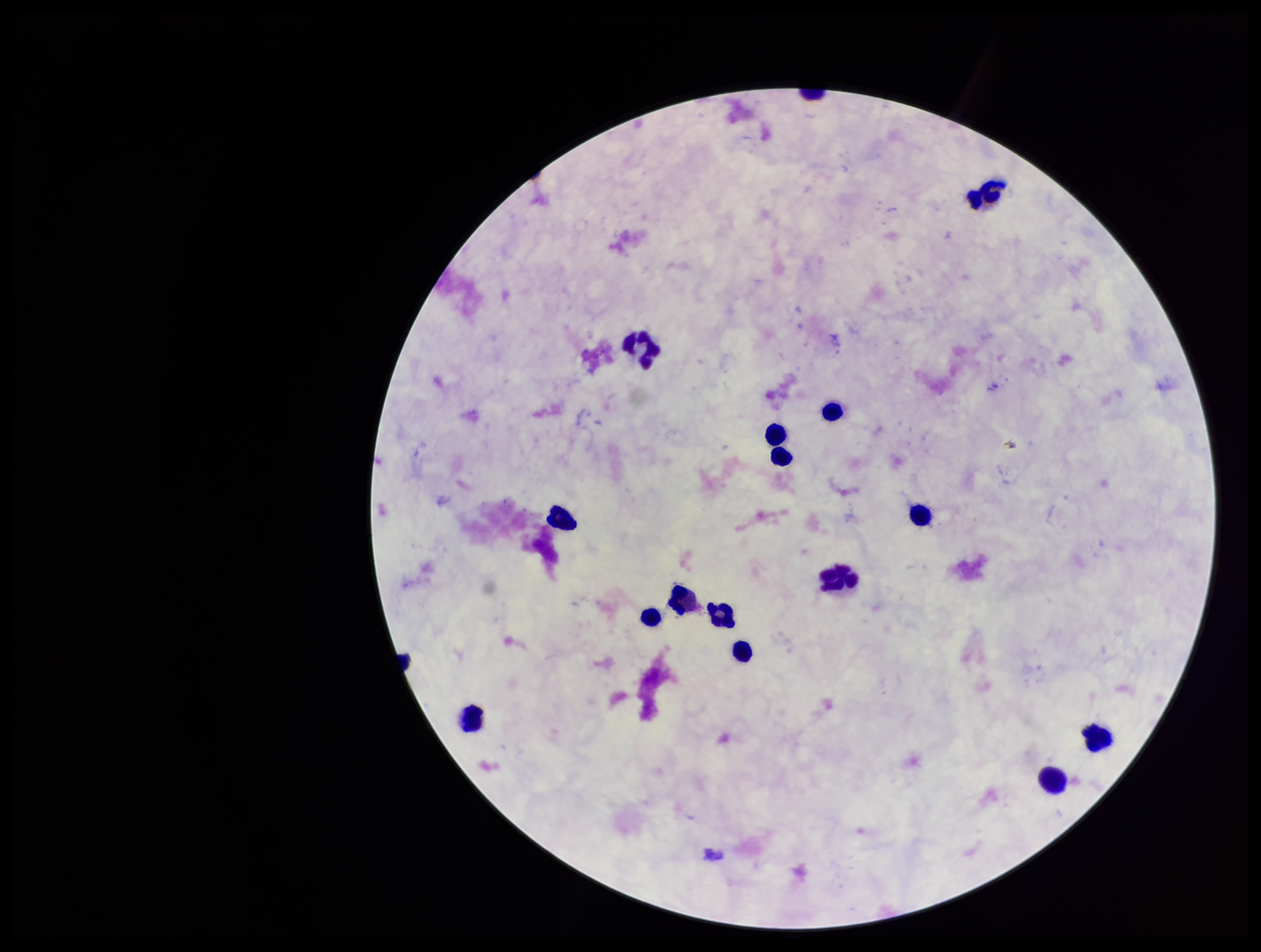 Single field of view. Leukocyte count: 15. Parasite count: 0. Preparation: thick blood smear. Image is 1261×952 pixels. Plasmodium parasites: none seen. Patient malaria status: negative. Smartphone photograph taken through the eyepiece of a microscope. Stained with Giemsa.